Point out each Plasmodium parasite.
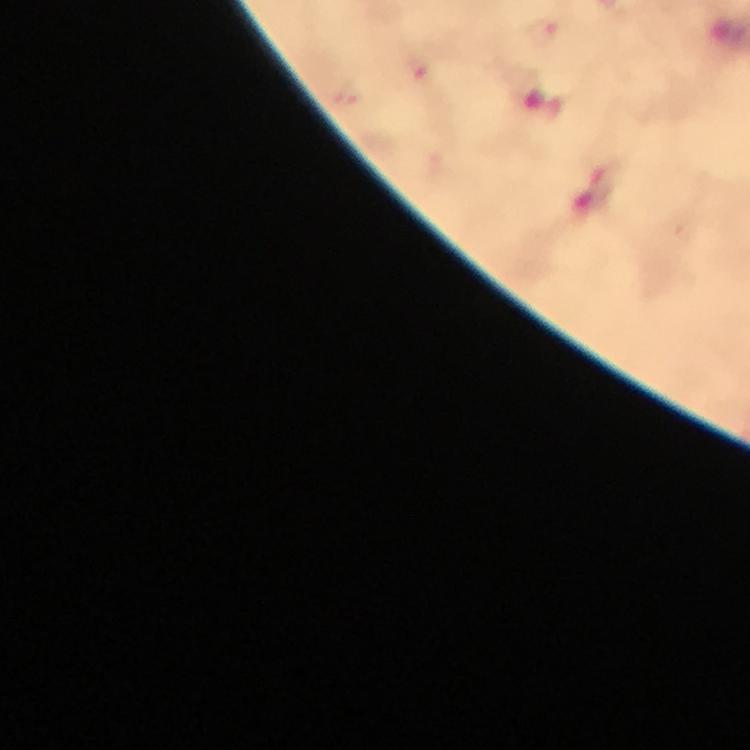
Approximate object centers, in pixels from the top-left corner.
Plasmodium parasites: (x=540, y=31).

Summary:
  - Stain: Giemsa
  - Context: from a malaria diagnostic workup
  - Cropped from: a single field of view
  - Magnification: 100x
  - Immersion oil: used
  - Preparation: thick smear
  - Capture: smartphone mounted on the microscope
  - Image size: 750×750 pixels